Comment on the morphology of the red blood cells.
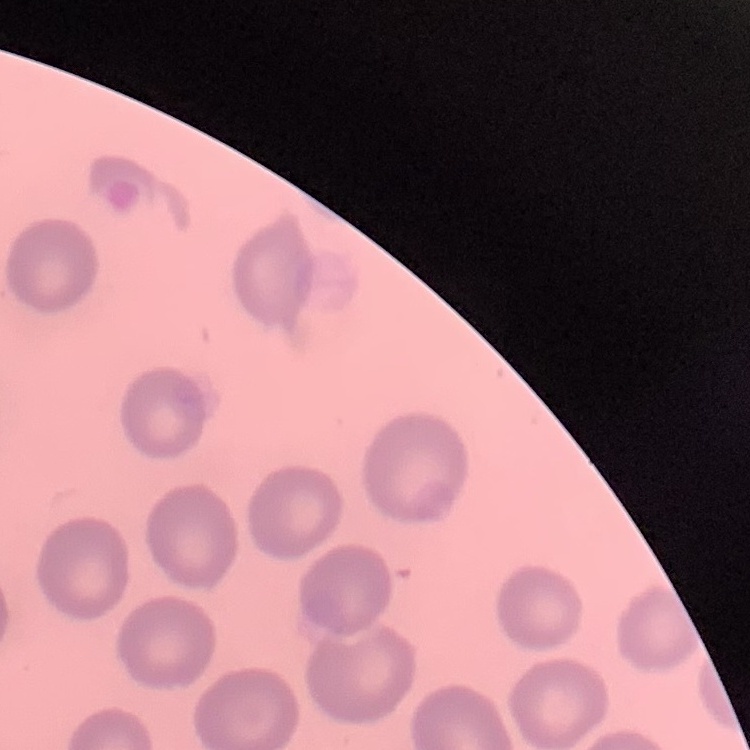
No rouleaux formation.

preparation = thin peripheral smear
image type = one tile cut from a larger photomicrograph
stain = Field's or Giemsa